Assess this cell for malaria.
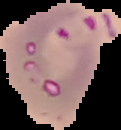
It is parasitized.

From a thin blood film. Image is 121×130 pixels. The area outside the segmented cell region is set to black.